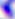

Summary:
  - Modality: photomicrograph
  - Identification: Toxoplasma gondii
  - Magnification: 400x